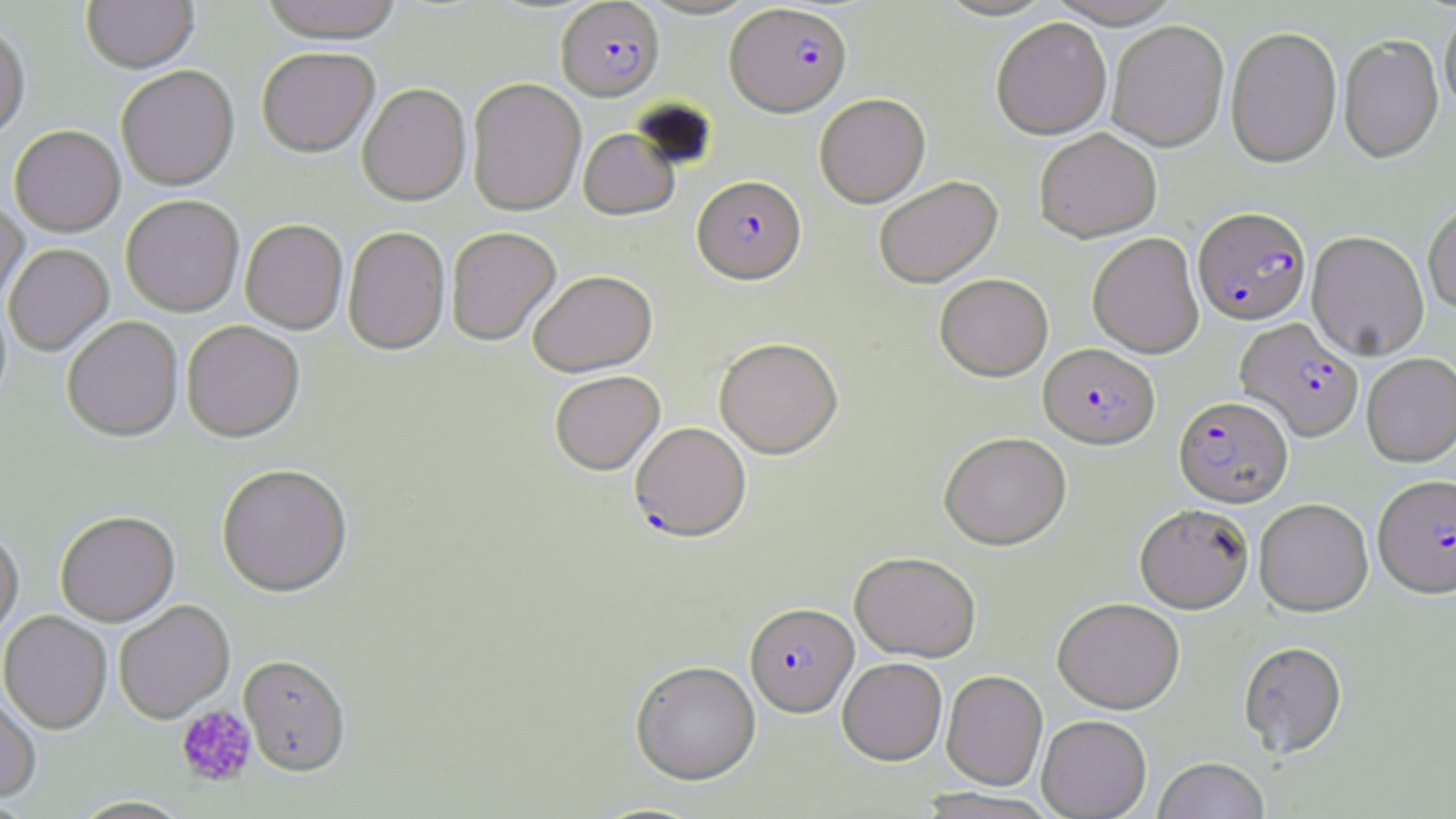
Summary:
  - Coordinate format: approximate bounding boxes as (x1, y1, x2, y2) in pixels
  - Platelet locations: (176, 704, 256, 787)
  - Uninfected red blood cell locations: (81, 0, 199, 76), (258, 0, 405, 45), (934, 0, 1058, 22), (1044, 0, 1186, 30), (1439, 8, 1456, 119), (991, 20, 1112, 140), (1107, 22, 1229, 152), (0, 24, 31, 142), (1225, 28, 1342, 170), (1339, 37, 1444, 164), (257, 48, 380, 159), (116, 67, 239, 192), (466, 78, 586, 216), (357, 84, 471, 206), (814, 94, 930, 208), (10, 127, 125, 239), (578, 128, 680, 221), (1035, 130, 1161, 242), (874, 176, 1003, 289), (121, 197, 244, 317), (0, 200, 29, 310), (1423, 200, 1456, 317), (240, 220, 348, 334), (342, 226, 450, 356), (446, 226, 561, 346), (1307, 232, 1429, 361), (1088, 233, 1204, 359), (4, 244, 114, 357), (528, 269, 658, 377), (935, 273, 1053, 381), (62, 317, 183, 443), (181, 321, 305, 443), (714, 337, 843, 459), (1361, 354, 1456, 468), (549, 370, 665, 475), (939, 431, 1071, 550), (216, 465, 353, 598), (1254, 499, 1372, 617), (1135, 504, 1254, 613), (55, 511, 180, 627), (0, 527, 24, 647), (850, 551, 981, 661), (1053, 598, 1185, 713), (114, 601, 234, 724), (0, 611, 112, 735), (1238, 640, 1348, 758), (238, 656, 351, 778), (837, 657, 947, 765), (631, 660, 761, 784), (942, 670, 1047, 790), (0, 688, 42, 804), (1037, 715, 1151, 818), (1153, 757, 1270, 819), (913, 788, 1059, 819), (68, 796, 195, 819)
  - Plasmodium falciparum-infected red blood cell locations: (557, 1, 664, 101), (725, 3, 852, 117), (692, 175, 806, 284), (1193, 207, 1312, 326), (1235, 319, 1363, 442), (1039, 343, 1160, 449), (1173, 395, 1293, 507), (630, 422, 751, 541), (1373, 476, 1456, 600), (744, 602, 858, 716)
  - Slide-level diagnosis: Plasmodium falciparum
  - Modality: light microscopy
  - Preparation: thin blood film
  - Field of view: one of a larger specimen
  - Magnification: 1000x
  - Image size: 1456×819 pixels
  - Stain: May-Grünwald-Giemsa